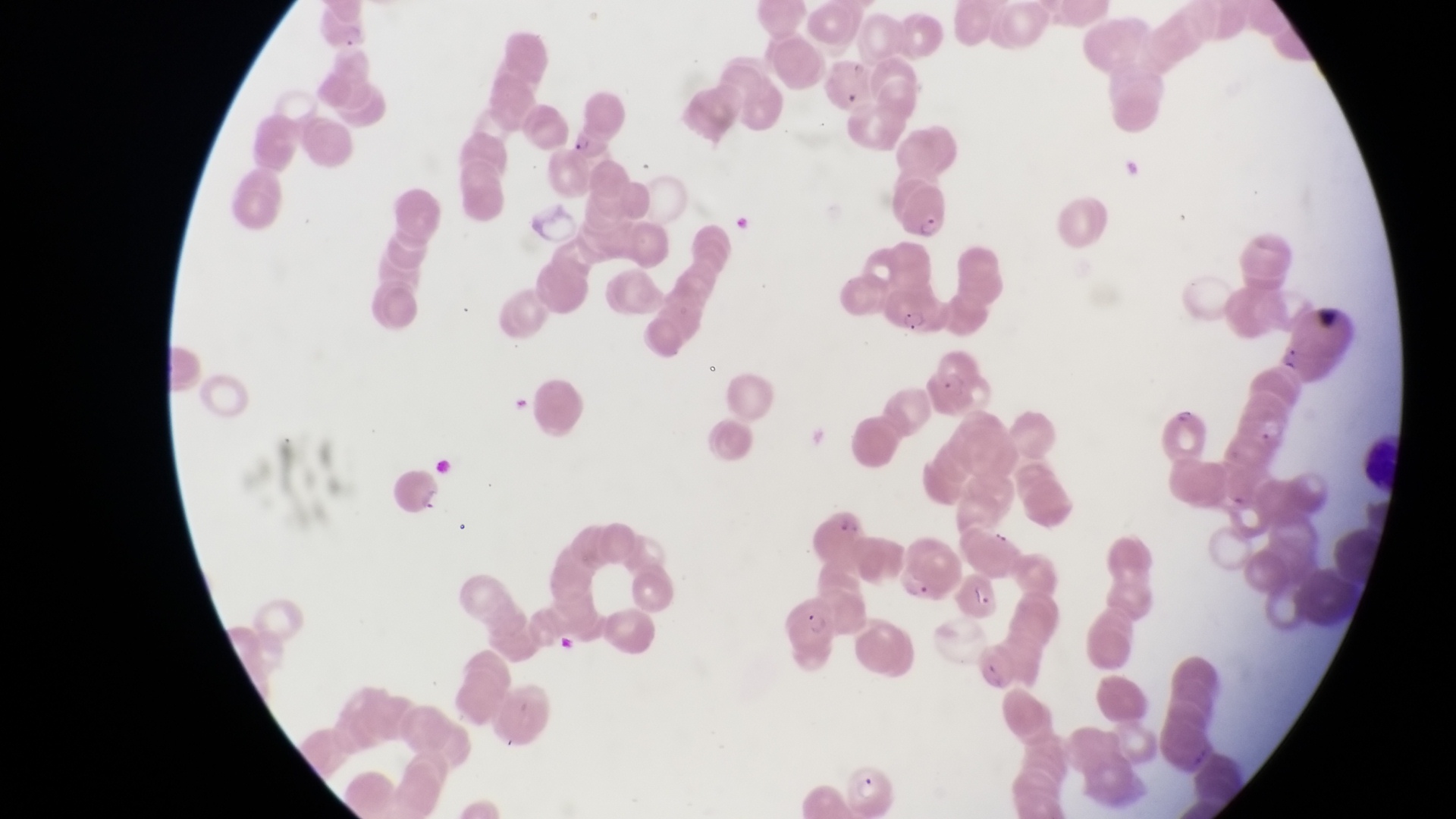
preparation: thin blood film
field_of_view: single
magnification: 1000x
capture: smartphone photograph through the eyepiece of an Olympus CX-23 microscope
image_size: 1456×819 pixels
country: Uganda
parasitised_red_blood_cell_locations: 'approximate bounding boxes as {left, top, right, bottom} in pixels: {561, 124, 610, 167}, {901, 175, 951, 238}, {890, 280, 949, 339}, {1229, 384, 1289, 455}, {392, 469, 450, 518}, {898, 544, 954, 610}, {948, 568, 997, 615}, {782, 592, 845, 663}'